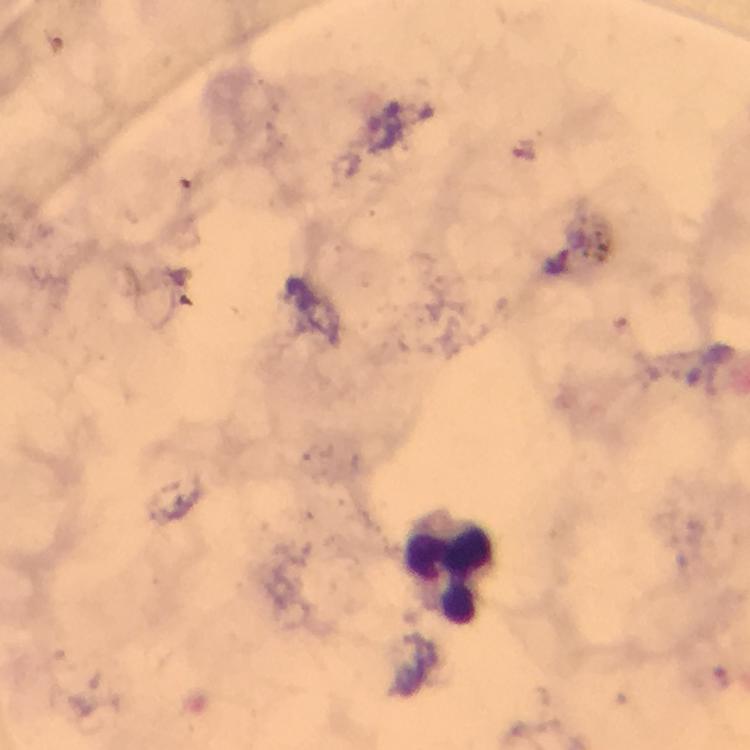 Approximate centers as {x, y} in pixels. Leukocyte locations: {446, 568}. Thick blood smear. Giemsa-stained preparation. From a diagnostic examination for malaria. Cropped region of a single field of view. 100x magnification. Photographed with a smartphone mounted on the microscope. Immersion oil was used. Image is 750×750 pixels. Malaria parasites: none detected.